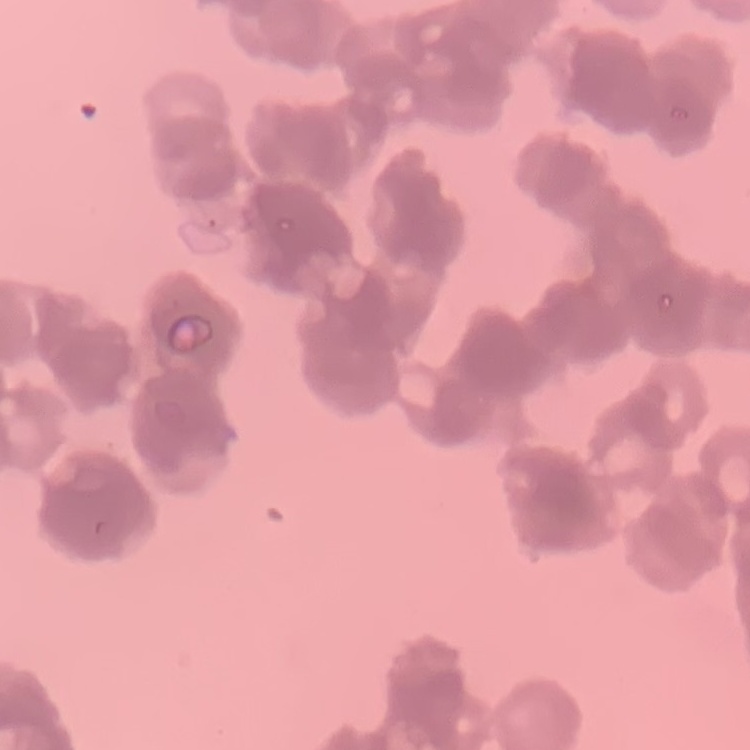
red blood cell morphology = rouleaux formation
stain = Field's or Giemsa
preparation = thin blood film
image type = square crop of a larger photomicrograph